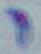

Summary:
  - Modality: photomicrograph
  - Magnification: 1000x
  - Identification: Toxoplasma gondii